State the preparation type.
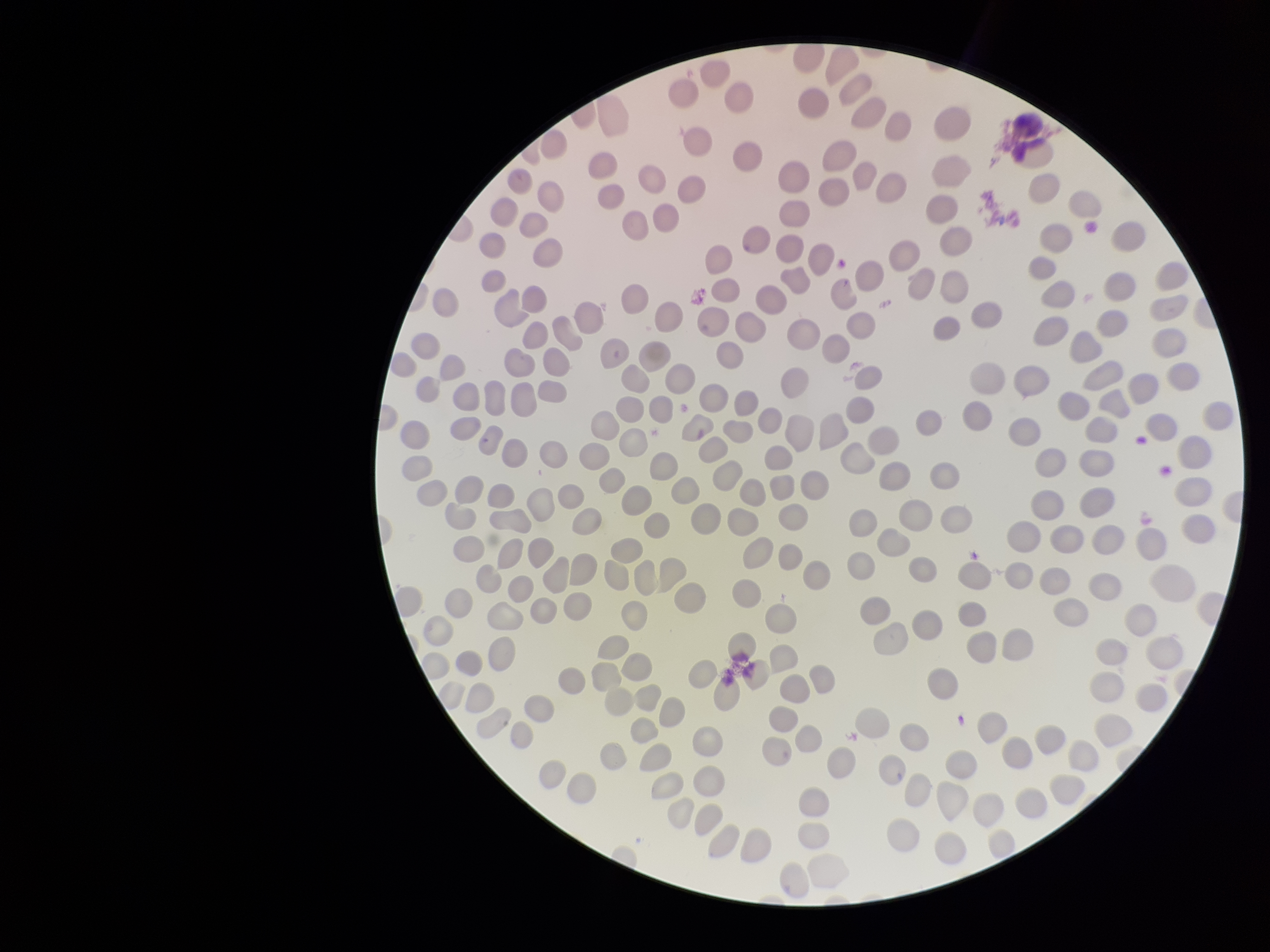

A thin smear.

Patient malaria status: negative. Parasitized red blood cell count: 0. One field from this slide. Red blood cell count: 246. Parasitized red blood cells: none identified. Smartphone photograph taken through the eyepiece of a microscope. Image is 1270×952 pixels. Giemsa stain.